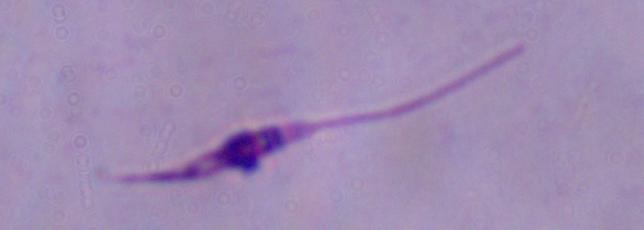

modality = photomicrograph
magnification = 1000x
identification = Leishmania